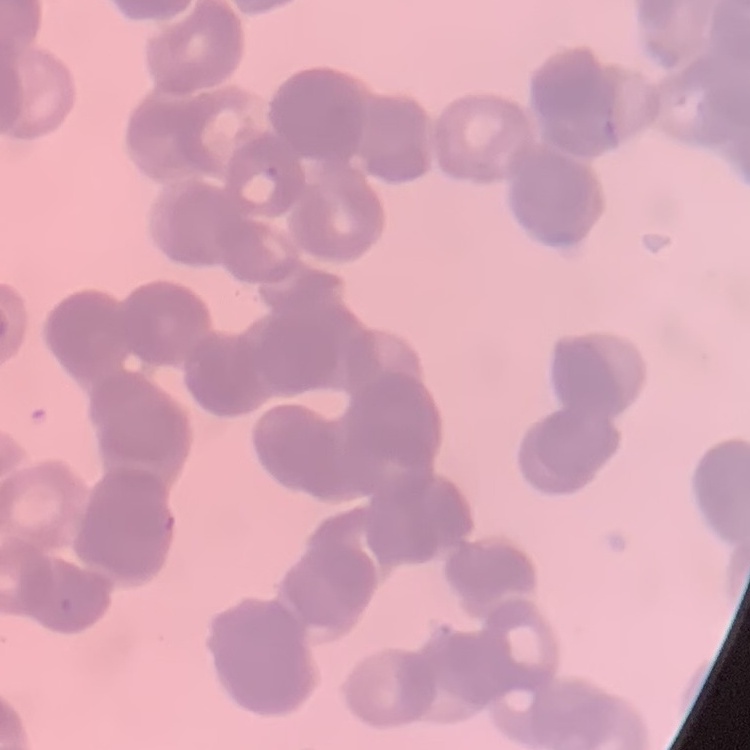

{
  "erythrocyte_morphology": "rouleaux formation",
  "stain": "Field's or Giemsa",
  "image_type": "square crop of a larger photomicrograph",
  "preparation": "thin blood film"
}